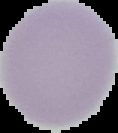
Summary:
  - Image type: cell region segmented out of the field of view; surrounding area masked to black
  - Image size: 118×133 pixels
  - Result: no Plasmodium parasites seen
  - Preparation: thin blood smear